Name the cell type shown.
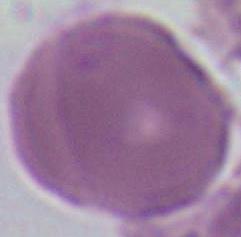
This is an erythrocyte.

Summary:
  - Modality: photomicrograph
  - Magnification: 1000x